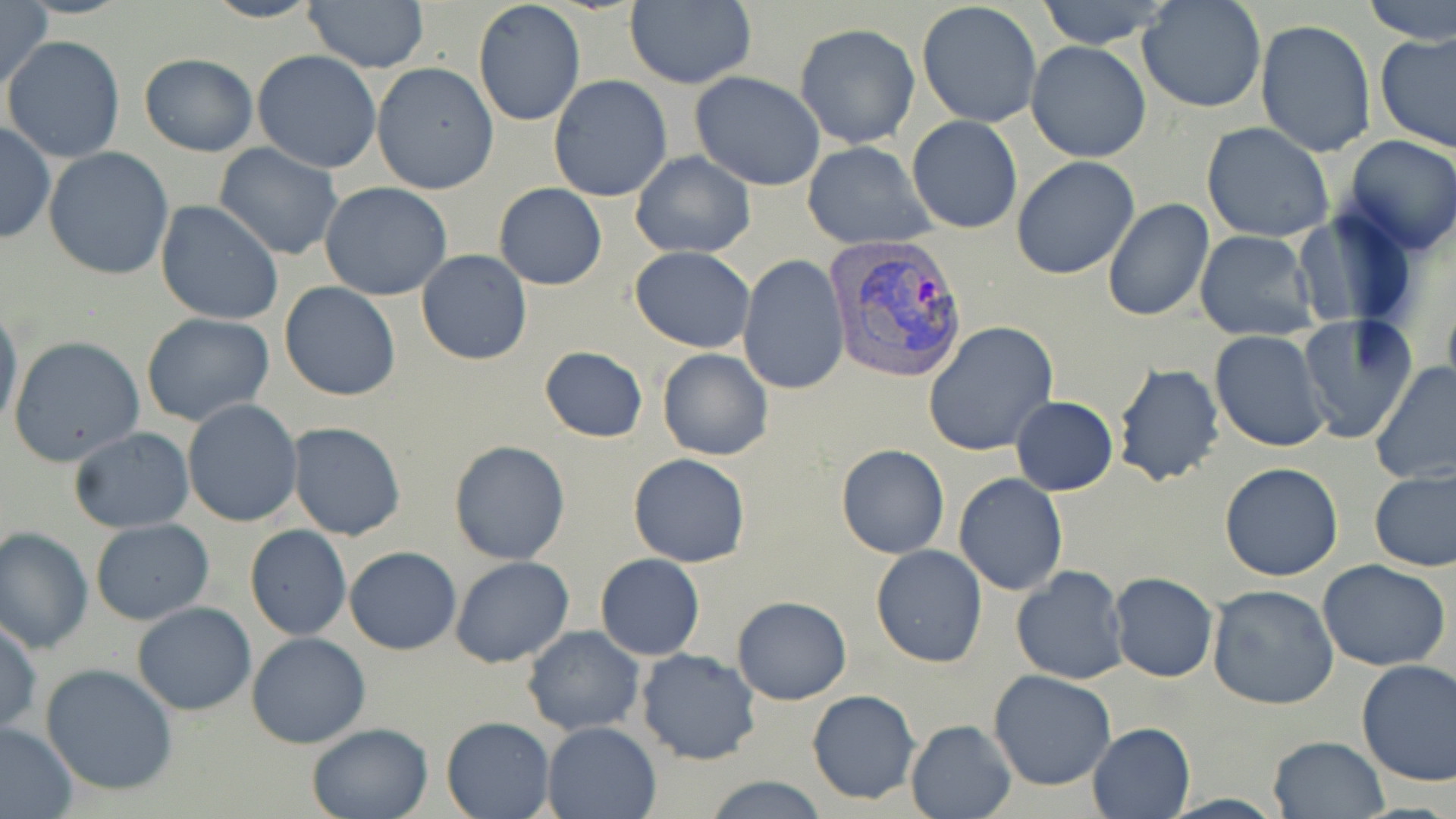

Approximate bounding boxes as (x1,y1)-(x2,y2) corner pairs in pixels. Uninfected red blood cell locations: (0,0)-(52,94), (200,0)-(324,24), (301,0)-(430,73), (472,0)-(586,128), (1036,0)-(1173,51), (1137,0)-(1266,113), (1365,0)-(1456,43), (624,2)-(755,88), (916,2)-(1042,129), (1255,19)-(1377,158), (795,23)-(920,150), (1377,31)-(1456,156), (3,35)-(127,161), (1026,41)-(1151,163), (252,50)-(382,174), (139,52)-(259,157), (371,63)-(498,195), (690,71)-(826,191), (548,75)-(674,203), (907,115)-(1023,235), (0,121)-(54,246), (1201,121)-(1335,243), (1340,135)-(1456,255), (801,141)-(936,251), (213,143)-(344,260), (43,147)-(175,281), (630,150)-(755,259), (1012,156)-(1141,280), (320,183)-(453,301), (493,183)-(606,290), (1101,197)-(1215,321), (155,199)-(284,326), (1292,209)-(1420,329), (1194,229)-(1320,342), (630,246)-(755,353), (416,249)-(531,364), (738,254)-(851,395), (280,282)-(400,401), (0,301)-(22,438), (140,312)-(274,426), (1296,312)-(1417,443), (922,321)-(1058,455), (1210,330)-(1331,453), (8,335)-(144,466), (539,346)-(648,443), (657,348)-(773,461), (1371,361)-(1456,485), (1111,362)-(1226,488), (1009,396)-(1119,496), (182,399)-(304,526), (288,421)-(406,540), (67,428)-(195,534), (448,440)-(570,565), (836,444)-(949,560), (627,454)-(751,568), (1220,463)-(1344,581), (1369,469)-(1456,573), (954,473)-(1068,594), (90,519)-(216,623), (245,524)-(351,640), (0,526)-(93,654), (871,544)-(987,669), (344,546)-(461,654), (596,554)-(706,660), (449,556)-(574,668), (1318,560)-(1452,672), (1010,567)-(1128,685), (1109,572)-(1219,682), (1206,584)-(1339,710), (733,596)-(852,704), (131,602)-(256,715), (0,616)-(42,738), (522,625)-(644,737), (246,633)-(371,749), (636,648)-(763,765), (1355,659)-(1456,785), (40,664)-(178,797), (987,670)-(1116,792), (807,690)-(920,804), (440,716)-(556,819), (904,719)-(1016,819), (305,721)-(435,819), (542,721)-(661,818), (1086,722)-(1195,817), (1,723)-(78,817), (1268,735)-(1389,818), (700,775)-(831,818). Plasmodium vivax-infected red blood cell locations: (821,233)-(965,379). Slide-level diagnosis: Plasmodium vivax. May-Grünwald-Giemsa stain. Image is 1456×819 pixels. Thin blood smear. 1000x magnification. Light microscopy. One field of a larger specimen.